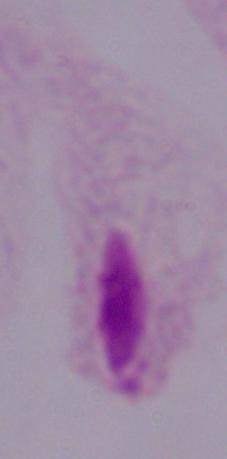
modality: micrograph
identification: trichomonad
magnification: 1000x